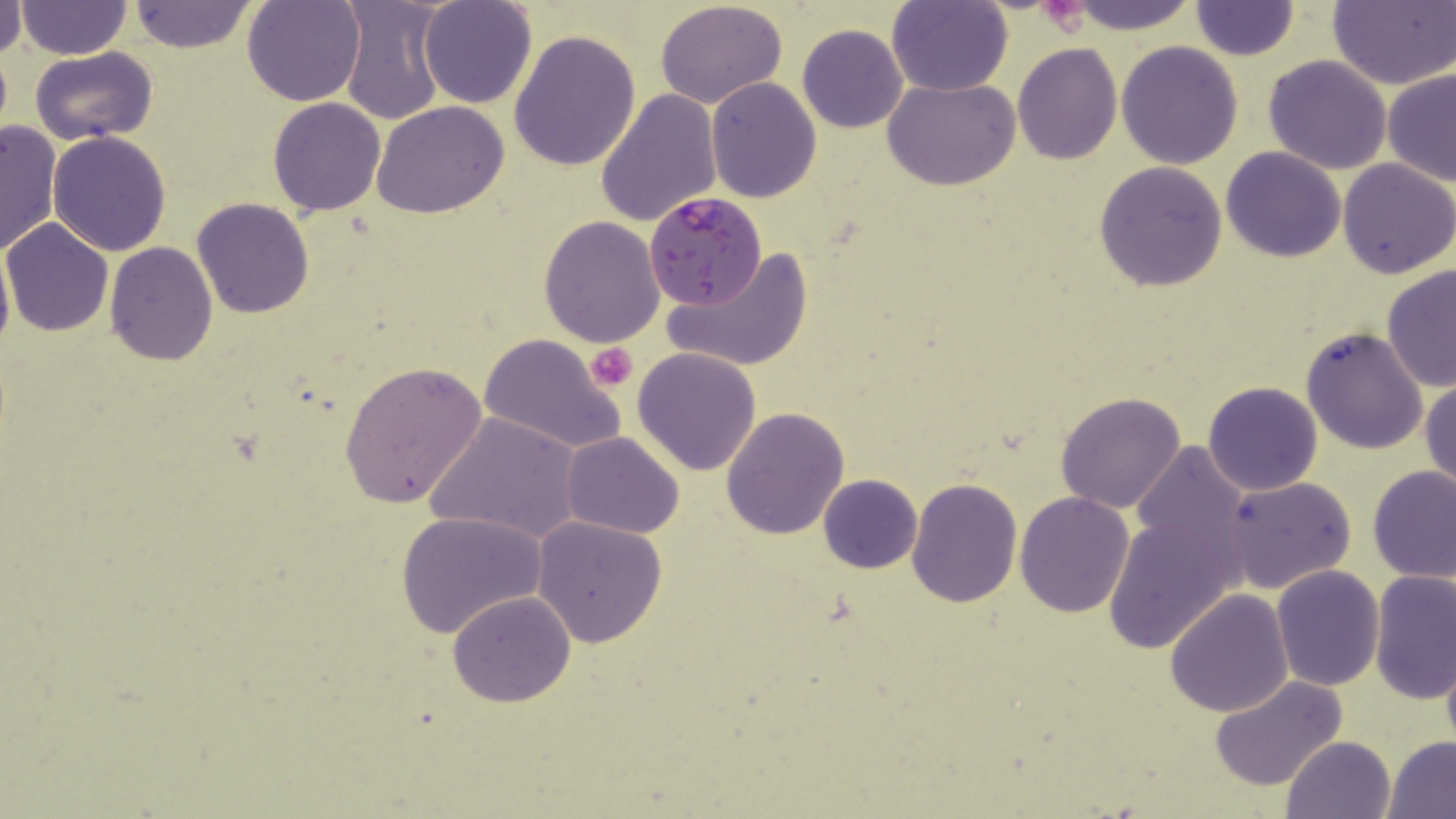
slide-level diagnosis = Plasmodium falciparum
stain = May-Grünwald-Giemsa
preparation = thin blood film
modality = light microscopy
platelet locations = approximate bounding boxes as named x1/y1/x2/y2 corners in pixels: (x1=585, y1=343, x2=638, y2=391)
image size = 1456×819 pixels
magnification = 1000x
field of view = single
uninfected red blood cell locations = approximate bounding boxes as named x1/y1/x2/y2 corners in pixels: (x1=127, y1=0, x2=257, y2=54), (x1=242, y1=0, x2=365, y2=106), (x1=337, y1=0, x2=448, y2=124), (x1=419, y1=0, x2=537, y2=109), (x1=655, y1=0, x2=787, y2=108), (x1=1062, y1=0, x2=1199, y2=33), (x1=17, y1=1, x2=130, y2=58), (x1=887, y1=1, x2=1012, y2=96), (x1=1329, y1=1, x2=1456, y2=89), (x1=0, y1=2, x2=27, y2=58), (x1=1190, y1=2, x2=1299, y2=61), (x1=797, y1=25, x2=908, y2=133), (x1=509, y1=28, x2=641, y2=172), (x1=1116, y1=40, x2=1243, y2=170), (x1=1012, y1=44, x2=1122, y2=165), (x1=29, y1=46, x2=158, y2=145), (x1=1263, y1=54, x2=1394, y2=174), (x1=1383, y1=69, x2=1456, y2=188), (x1=705, y1=76, x2=821, y2=203), (x1=884, y1=78, x2=1022, y2=189), (x1=595, y1=89, x2=723, y2=228), (x1=267, y1=98, x2=388, y2=217), (x1=373, y1=100, x2=512, y2=218), (x1=0, y1=118, x2=63, y2=257), (x1=47, y1=131, x2=172, y2=256), (x1=1221, y1=147, x2=1345, y2=262), (x1=1337, y1=159, x2=1455, y2=278), (x1=1094, y1=160, x2=1228, y2=293), (x1=192, y1=197, x2=313, y2=318), (x1=538, y1=216, x2=666, y2=348), (x1=2, y1=218, x2=114, y2=336), (x1=0, y1=238, x2=13, y2=367), (x1=104, y1=241, x2=218, y2=366), (x1=667, y1=247, x2=814, y2=373), (x1=1382, y1=264, x2=1456, y2=393), (x1=1301, y1=325, x2=1431, y2=456), (x1=478, y1=334, x2=624, y2=454), (x1=631, y1=347, x2=762, y2=477), (x1=339, y1=360, x2=486, y2=510), (x1=1421, y1=375, x2=1456, y2=492), (x1=1203, y1=380, x2=1323, y2=496), (x1=1055, y1=391, x2=1188, y2=514), (x1=722, y1=406, x2=850, y2=541), (x1=424, y1=409, x2=583, y2=545), (x1=561, y1=432, x2=685, y2=538), (x1=1133, y1=440, x2=1249, y2=559), (x1=1367, y1=466, x2=1456, y2=585), (x1=817, y1=473, x2=923, y2=574), (x1=1223, y1=477, x2=1356, y2=594), (x1=905, y1=478, x2=1023, y2=609), (x1=1014, y1=491, x2=1134, y2=617), (x1=394, y1=511, x2=549, y2=639), (x1=1102, y1=513, x2=1241, y2=653), (x1=531, y1=516, x2=668, y2=647), (x1=1271, y1=566, x2=1384, y2=690), (x1=1369, y1=570, x2=1454, y2=706), (x1=447, y1=591, x2=575, y2=708), (x1=1165, y1=591, x2=1293, y2=717), (x1=1208, y1=674, x2=1352, y2=793), (x1=1281, y1=735, x2=1397, y2=819), (x1=1382, y1=736, x2=1456, y2=818)
Plasmodium falciparum-infected red blood cell locations = approximate bounding boxes as named x1/y1/x2/y2 corners in pixels: (x1=644, y1=193, x2=766, y2=310)